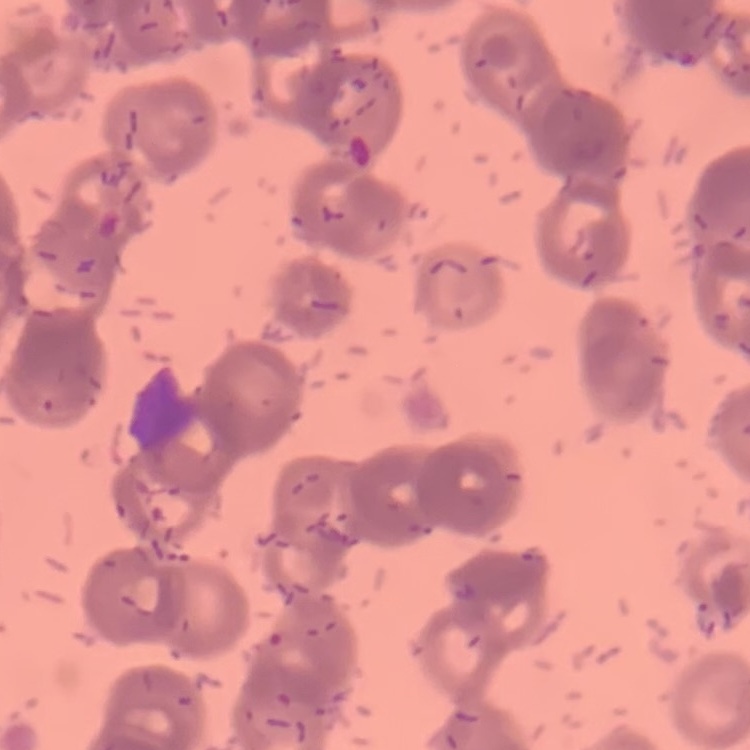

The erythrocytes show rouleaux formation. Field's or Giemsa stain. One tile cut from a larger photomicrograph. Thin blood film.